Report the malaria status of this cell.
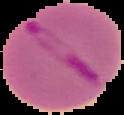
It is parasitized.

From a thin blood film. Image is 124×115 pixels. Cell region segmented out of the field of view; the surrounding area is masked to black.